Assess this cell for malaria.
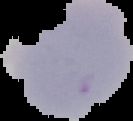
It is uninfected.

{
  "image_type": "segmented cell region on a black background",
  "image_size": "133×121 pixels",
  "preparation": "thin blood film"
}